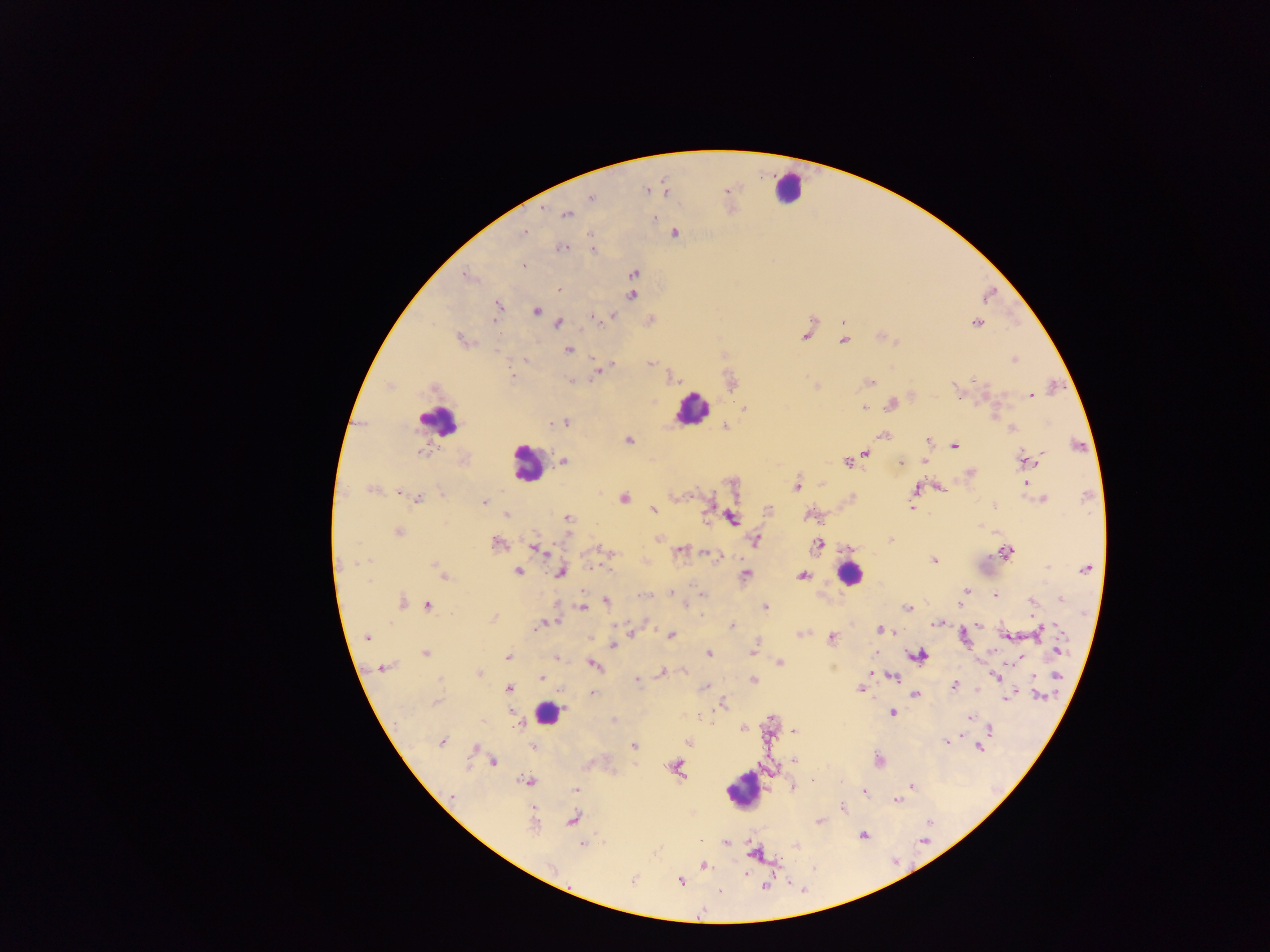
{
  "preparation": "thick blood film",
  "field_of_view": "single",
  "country": "Ghana",
  "capture": "mobile-phone photograph through a microscope",
  "malaria_parasite_locations": "approximate centers as {x, y} in pixels: {646, 191}, {666, 192}, {591, 197}, {543, 206}, {567, 215}, {654, 219}, {524, 231}, {674, 233}, {563, 247}, {594, 250}, {524, 266}, {633, 273}, {468, 277}, {558, 288}, {631, 295}, {498, 306}, {536, 311}, {613, 316}, {593, 317}, {559, 323}, {976, 323}, {806, 334}, {461, 339}, {844, 340}, {568, 350}, {1014, 359}, {527, 360}, {650, 364}, {598, 371}, {511, 376}, {572, 381}, {870, 382}, {1031, 395}, {890, 404}, {864, 407}, {745, 408}, {550, 422}, {565, 423}, {725, 427}, {1012, 428}, {883, 435}, {628, 440}, {928, 441}, {955, 446}, {420, 452}, {865, 454}, {1042, 454}, {1034, 457}, {1026, 460}, {564, 461}, {847, 462}, {899, 462}, {925, 462}, {969, 473}, {1026, 483}, {796, 485}, {941, 488}, {916, 490}, {371, 491}, {399, 492}, {690, 496}, {623, 497}, {418, 498}, {1043, 499}, {483, 502}, {911, 507}, {652, 509}, {808, 514}, {506, 515}, {567, 518}, {732, 518}, {398, 532}, {658, 538}, {891, 539}, {755, 540}, {497, 544}, {818, 544}, {536, 549}, {681, 549}, {602, 550}, {1007, 551}, {708, 553}, {933, 561}, {364, 562}, {434, 565}, {1085, 569}, {439, 570}, {518, 572}, {561, 572}, {746, 575}, {444, 576}, {803, 576}, {966, 591}, {671, 593}, {702, 594}, {645, 595}, {995, 596}, {1060, 600}, {606, 602}, {1031, 602}, {402, 603}, {428, 605}, {686, 605}, {583, 607}, {765, 607}, {907, 609}, {494, 618}, {546, 623}, {937, 624}, {979, 624}, {541, 625}, {732, 626}, {1048, 628}, {880, 629}, {887, 632}, {1038, 632}, {670, 635}, {799, 635}, {963, 636}, {1006, 636}, {367, 637}, {831, 637}, {614, 644}, {1058, 651}, {753, 652}, {425, 653}, {709, 653}, {918, 656}, {507, 657}, {556, 658}, {1018, 658}, {780, 663}, {594, 665}, {383, 668}, {684, 671}, {663, 672}, {479, 673}, {995, 676}, {1056, 676}, {893, 677}, {542, 679}, {753, 680}, {637, 681}, {955, 685}, {704, 687}, {509, 689}, {861, 689}, {591, 693}, {1014, 694}, {916, 696}, {1040, 696}, {1009, 697}, {436, 702}, {722, 704}, {892, 712}, {969, 716}, {613, 721}, {517, 725}, {743, 728}, {989, 729}, {795, 731}, {947, 741}, {442, 742}, {688, 743}, {635, 746}, {533, 747}, {979, 748}, {473, 749}, {794, 760}, {493, 762}, {676, 766}, {813, 779}, {525, 780}, {911, 787}, {793, 788}, {576, 790}, {865, 792}, {452, 795}, {896, 800}, {843, 807}, {572, 819}, {820, 821}, {535, 824}, {863, 835}, {725, 842}, {582, 844}, {754, 853}, {704, 865}, {633, 880}, {680, 881}, {765, 886}, {720, 891}",
  "image_size": "1270×952 pixels",
  "leukocyte_locations": "approximate centers as {x, y} in pixels: {787, 188}, {690, 409}, {439, 421}, {526, 463}, {849, 575}, {547, 714}, {742, 790}"
}